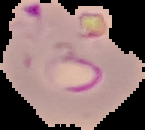
result: malaria parasites identified
image_type: segmented cell region on a black background
preparation: thin blood smear
image_size: 145×130 pixels